Comment on the morphology of the erythrocytes.
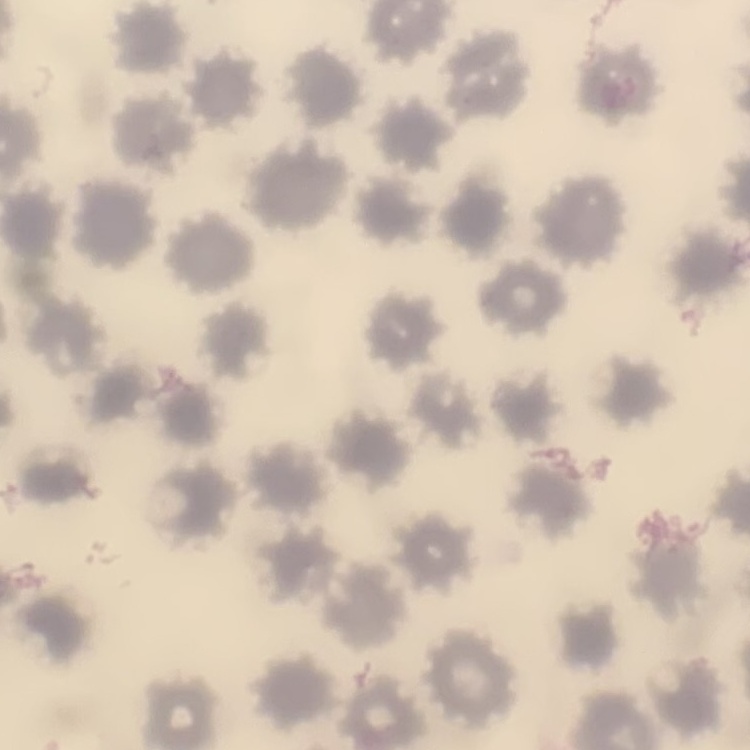

They show no rouleaux formation.

Square crop of a larger photomicrograph. Field's or Giemsa stain. Thin peripheral smear.